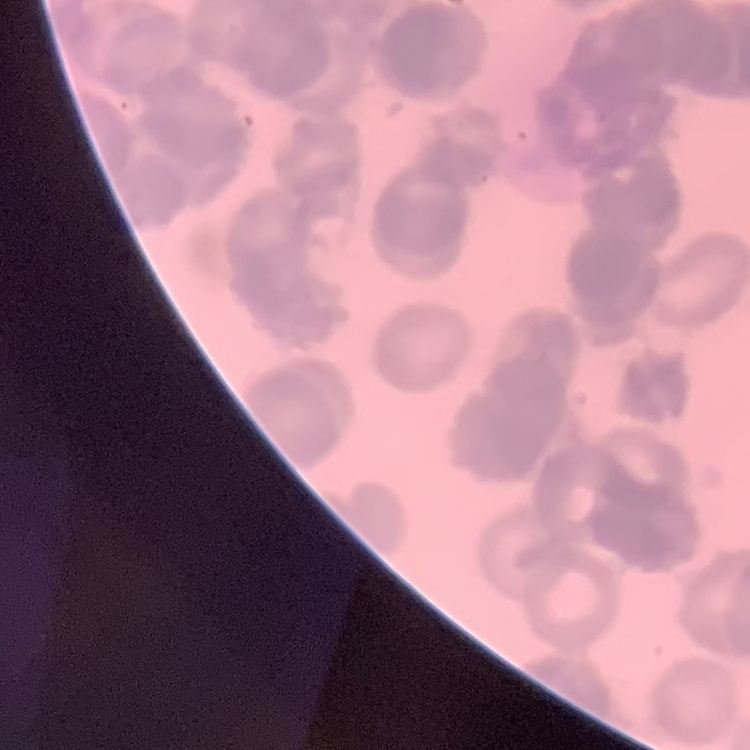 The erythrocytes exhibit rouleaux formation. Field's or Giemsa stain. Thin peripheral smear. One tile cut from a larger photomicrograph.